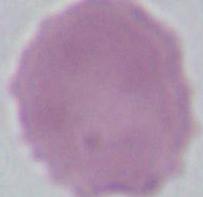

magnification = 1000x
modality = micrograph
identification = erythrocyte